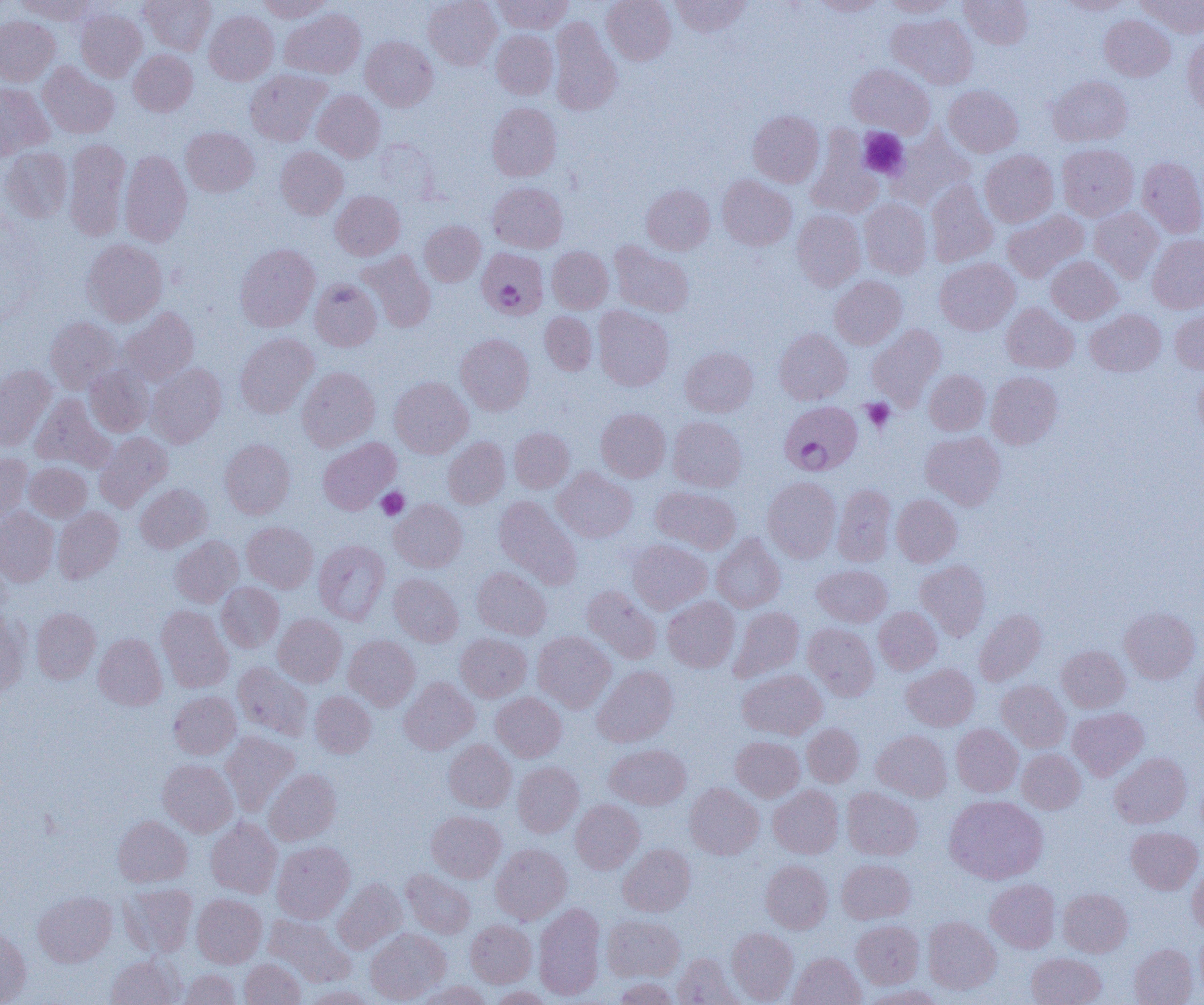

Summary:
  - Coordinate format: approximate bounding boxes as (x1,y1)-(x2,y2) corner pairs in pixels
  - Platelet locations: (858,128)-(908,179), (862,399)-(895,433), (376,487)-(408,520)
  - Uninfected red blood cell locations: (16,0)-(96,24), (139,0)-(215,55), (258,0)-(331,21), (423,0)-(501,70), (492,0)-(572,33), (602,0)-(676,65), (670,0)-(752,37), (812,0)-(887,17), (881,0)-(958,17), (959,0)-(1033,49), (1139,0)-(1204,37), (1058,1)-(1134,15), (281,8)-(365,78), (76,9)-(147,82), (204,10)-(278,85), (887,14)-(978,88), (0,15)-(60,86), (1099,15)-(1175,81), (549,17)-(621,116), (491,30)-(558,99), (1182,34)-(1204,113), (361,36)-(438,111), (129,49)-(198,116), (38,63)-(119,139), (846,64)-(934,139), (245,69)-(331,146), (1048,75)-(1132,146), (0,83)-(53,158), (944,85)-(1022,157), (312,90)-(385,162), (487,102)-(562,181), (748,110)-(825,187), (181,127)-(258,197), (889,131)-(973,208), (807,133)-(882,218), (64,138)-(131,241), (372,139)-(439,202), (1057,143)-(1139,221), (276,146)-(347,219), (1,147)-(72,223), (119,150)-(192,247), (980,150)-(1058,227), (1137,156)-(1204,238), (717,175)-(797,250), (926,180)-(998,268), (488,182)-(567,252), (642,184)-(714,254), (331,191)-(405,260), (860,199)-(931,278), (1089,207)-(1163,282), (791,209)-(865,291), (1002,210)-(1089,283), (419,221)-(485,286), (1147,234)-(1204,314), (82,239)-(168,325), (609,242)-(693,318), (235,243)-(319,331), (547,247)-(613,313), (358,250)-(436,332), (1046,256)-(1122,324), (934,258)-(1019,335), (830,275)-(906,349), (310,279)-(381,351), (1001,303)-(1078,373), (593,306)-(674,391), (1170,306)-(1204,373), (119,308)-(200,386), (1086,309)-(1166,376), (540,311)-(596,375), (46,317)-(123,393), (867,324)-(945,408), (775,329)-(852,404), (235,332)-(318,417), (456,333)-(534,415), (680,347)-(758,416), (146,363)-(227,447), (85,364)-(154,436), (0,365)-(55,449), (297,367)-(379,451), (1193,368)-(1204,442), (924,369)-(989,436), (986,372)-(1063,449), (389,376)-(473,458), (30,394)-(113,471), (596,408)-(670,482), (668,416)-(747,492), (509,427)-(574,492), (921,431)-(1006,510), (95,432)-(173,511), (443,437)-(509,508), (318,438)-(400,515), (220,439)-(295,518), (0,454)-(33,522), (25,462)-(92,521), (552,467)-(637,542), (762,477)-(841,562), (135,484)-(211,553), (832,484)-(897,566), (652,487)-(741,554), (892,494)-(962,566), (494,496)-(581,589), (390,499)-(467,572), (53,507)-(124,583), (0,508)-(59,587), (242,521)-(318,592), (711,534)-(785,612), (170,536)-(243,607), (628,539)-(711,613), (313,540)-(390,624), (915,559)-(990,641), (812,564)-(892,626), (472,567)-(552,639), (389,573)-(463,646), (217,582)-(284,652), (582,586)-(661,664), (663,596)-(739,672), (156,605)-(233,692), (729,607)-(804,682), (874,607)-(942,674), (31,608)-(101,684), (1120,608)-(1200,684), (0,609)-(29,695), (974,609)-(1046,685), (273,614)-(346,686), (803,623)-(879,699), (533,631)-(616,713), (93,633)-(167,710), (456,633)-(531,701), (344,635)-(420,710), (1057,645)-(1130,712), (1191,655)-(1204,734), (233,662)-(313,740), (902,663)-(979,731), (592,665)-(678,747), (737,669)-(826,739), (399,677)-(479,754), (997,680)-(1070,751), (169,691)-(241,759), (310,691)-(376,757), (491,692)-(566,761), (1068,707)-(1148,780), (802,723)-(863,786), (951,724)-(1022,797), (872,730)-(952,801), (221,731)-(299,816), (732,736)-(804,802), (443,740)-(516,812), (605,744)-(691,809), (1017,749)-(1085,813), (1109,752)-(1191,828), (158,760)-(237,836), (513,762)-(583,837), (264,769)-(341,845), (685,783)-(763,859), (768,785)-(843,858), (842,787)-(922,860), (944,795)-(1047,883), (571,799)-(644,873), (426,811)-(505,882), (113,815)-(192,887), (206,818)-(282,898), (1127,827)-(1203,894), (272,840)-(354,923), (491,843)-(572,924), (610,843)-(688,982), (618,843)-(695,916), (837,858)-(915,923), (760,860)-(832,933), (1187,862)-(1204,936), (401,869)-(475,938), (333,878)-(406,953), (985,879)-(1060,952), (121,883)-(197,957), (1058,888)-(1132,957), (33,891)-(116,967), (192,894)-(266,968), (534,902)-(605,1000), (264,914)-(355,987), (603,915)-(685,981), (923,917)-(1001,994), (465,919)-(536,987), (851,920)-(924,989), (0,926)-(31,1004), (365,927)-(450,1004), (727,927)-(798,1003), (1196,927)-(1204,999), (1129,943)-(1198,1005), (788,952)-(865,1005), (1027,952)-(1106,1005), (106,954)-(185,1005), (672,954)-(740,1005), (240,959)-(306,1005), (177,970)-(241,1005), (613,977)-(679,1005), (414,981)-(492,1005), (860,984)-(945,1005), (302,985)-(377,1005), (487,986)-(555,1004)
  - Plasmodium falciparum-infected red blood cell locations: (477,248)-(548,319), (779,401)-(862,475)
  - Slide-level diagnosis: Plasmodium falciparum
  - Field of view: single
  - Preparation: thin blood film
  - Image size: 1204×1005 pixels
  - Magnification: 1000x
  - Modality: optical microscopy